Report the malaria status of this cell.
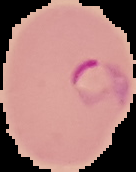

It is parasitized.

{
  "image_type": "segmented cell region with the area outside set to black",
  "preparation": "thin blood smear",
  "image_size": "136×172 pixels"
}